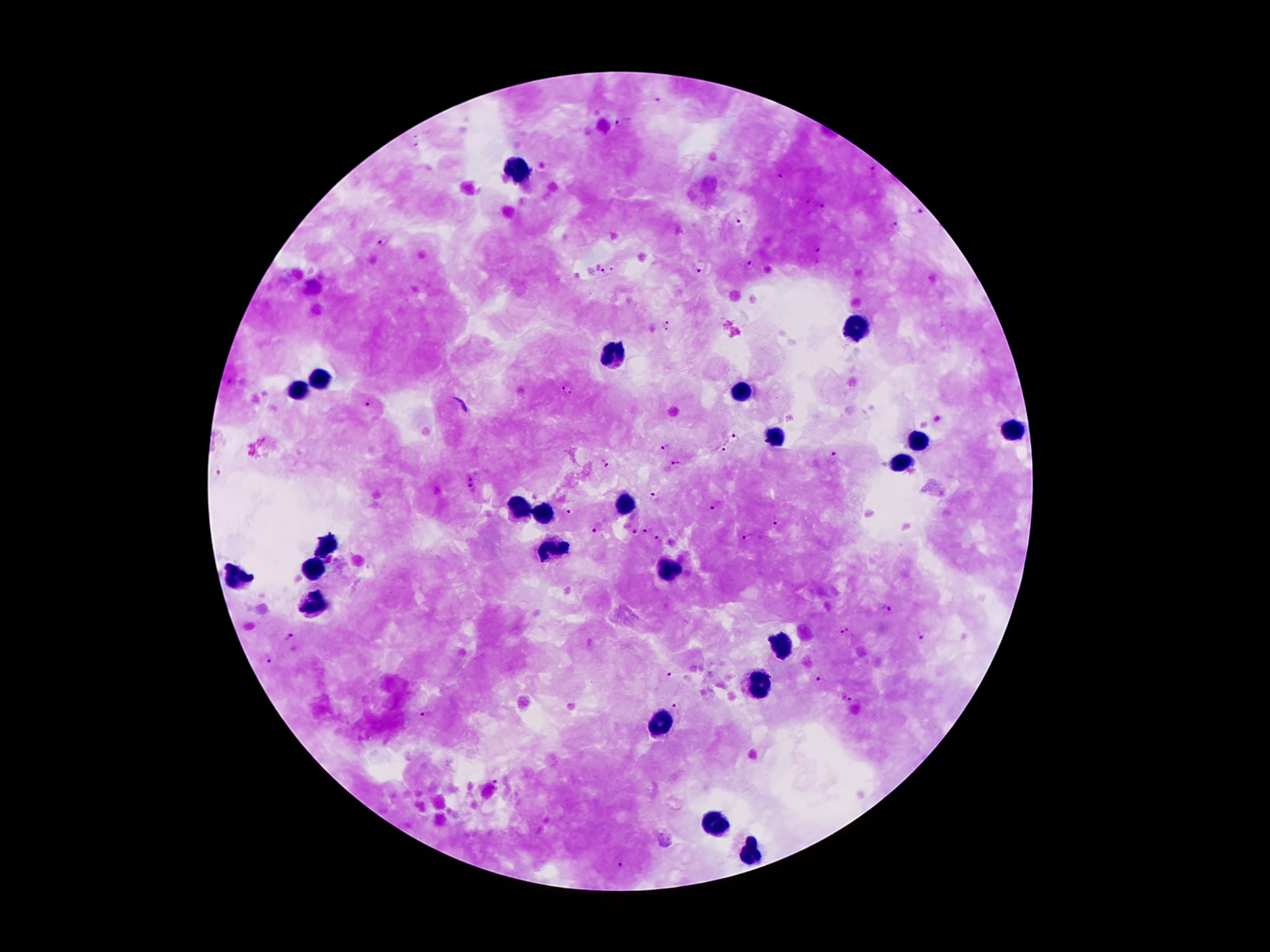
coordinate format = approximate centers as (x, y) in pixels
malaria parasite locations = (657, 101), (620, 123), (416, 141), (873, 170), (780, 176), (821, 203), (920, 210), (739, 224), (895, 226), (385, 239), (817, 250), (750, 265), (701, 266), (607, 270), (666, 324), (567, 388), (368, 402), (736, 438), (665, 446), (724, 448), (834, 455), (676, 462), (605, 464), (216, 471), (469, 475), (470, 487), (656, 497), (718, 506), (570, 510), (777, 521), (595, 529), (645, 531), (631, 532), (747, 537), (659, 540), (886, 609), (846, 631), (288, 636), (920, 637), (268, 657), (670, 673), (819, 679), (847, 697), (676, 703), (426, 713), (497, 782), (617, 860)
leukocyte locations = (520, 170), (856, 327), (608, 353), (320, 378), (297, 388), (740, 391), (1016, 433), (779, 437), (917, 437), (905, 464), (625, 505), (520, 511), (547, 513), (322, 547), (551, 553), (316, 567), (669, 571), (240, 576), (315, 604), (779, 647), (760, 685), (661, 722), (715, 826), (753, 852)
patient malaria status = positive for Plasmodium falciparum
preparation = thick blood smear
field of view = single
stain = Giemsa
capture = smartphone camera through the microscope eyepiece
image size = 1270×952 pixels
magnification = 100x